Locate and identify every blood parasite.
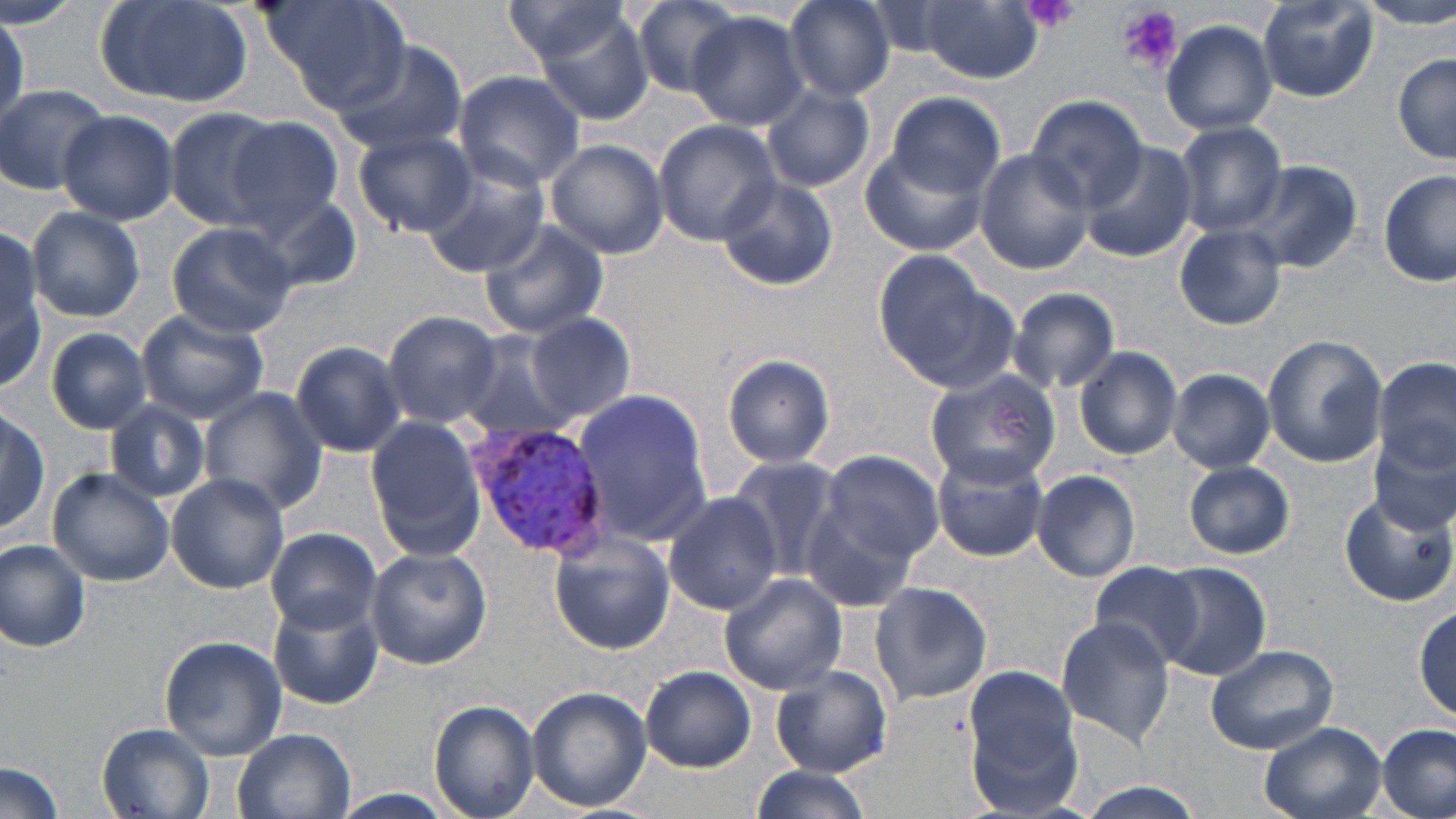
Approximate bounding boxes as (x1,y1)-(x2,y2) corner pairs in pixels.
Plasmodium vivax-infected red blood cells: (469,421)-(611,558).
No Plasmodium falciparum, Plasmodium ovale, Plasmodium malariae, Babesia divergens, or Trypanosoma brucei observed.

Platelet locations: (1020,0)-(1083,32), (1117,6)-(1182,73). Uninfected red blood cell locations: (93,0)-(255,112), (261,0)-(412,112), (630,0)-(742,98), (783,0)-(896,101), (1256,0)-(1379,104), (1360,0)-(1456,30), (498,1)-(640,74), (864,2)-(962,61), (920,2)-(1046,83), (520,5)-(658,127), (0,11)-(25,134), (686,11)-(810,131), (1161,19)-(1278,135), (329,38)-(471,157), (1392,54)-(1455,164), (454,69)-(586,190), (1,85)-(111,196), (763,86)-(874,193), (886,90)-(1005,194), (1026,96)-(1148,211), (167,106)-(290,233), (57,109)-(177,224), (228,114)-(347,226), (652,119)-(780,246), (1172,121)-(1286,237), (1119,126)-(1253,262), (46,130)-(164,303), (352,130)-(476,236), (545,139)-(668,259), (1080,142)-(1194,261), (863,143)-(987,255), (973,149)-(1094,274), (418,161)-(552,278), (1234,162)-(1361,275), (1379,170)-(1456,288), (716,177)-(838,290), (247,188)-(363,291), (26,206)-(145,322), (476,218)-(609,340), (165,222)-(297,338), (1174,224)-(1285,329), (0,235)-(46,388), (870,250)-(1001,383), (1004,285)-(1121,393), (138,311)-(269,422), (382,311)-(503,427), (526,313)-(634,424), (46,328)-(152,435), (457,332)-(577,443), (1261,334)-(1388,468), (287,341)-(409,460), (1075,345)-(1183,460), (721,353)-(835,469), (1369,357)-(1453,496), (922,368)-(1060,490), (1169,368)-(1274,472), (199,389)-(327,517), (571,389)-(713,546), (104,401)-(211,503), (0,405)-(48,536), (362,419)-(487,563), (1370,437)-(1453,539), (930,446)-(1050,562), (819,448)-(944,566), (726,456)-(844,583), (1183,461)-(1295,560), (46,468)-(175,587), (1031,470)-(1141,582), (167,473)-(290,594), (1337,489)-(1455,607), (662,493)-(780,615), (799,493)-(928,612), (265,527)-(379,633), (549,536)-(674,655), (1,540)-(93,651), (364,546)-(491,669), (1089,560)-(1208,670), (1153,562)-(1272,681), (719,574)-(846,695), (868,580)-(993,707), (268,595)-(382,710), (1414,603)-(1455,720), (1057,616)-(1174,746), (159,636)-(287,759), (1204,642)-(1338,755), (961,663)-(1086,816), (639,666)-(755,772), (771,666)-(892,776), (526,686)-(651,813), (428,700)-(538,819), (1258,721)-(1386,819), (1376,722)-(1456,819), (95,723)-(215,819), (233,729)-(355,818), (1,760)-(66,819), (748,764)-(873,818), (1073,784)-(1211,818), (333,789)-(460,819). Slide-level diagnosis: Plasmodium vivax. Optical microscopy. 1000x magnification. Single field of view. May-Grünwald-Giemsa-stained preparation. Thin blood smear. Image is 1456×819 pixels.